Classify this cell by malaria status.
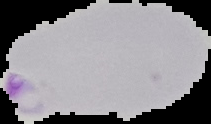

It is parasitized.

Summary:
  - Image type: segmented cell region with the area outside set to black
  - Image size: 211×124 pixels
  - Preparation: thin blood film